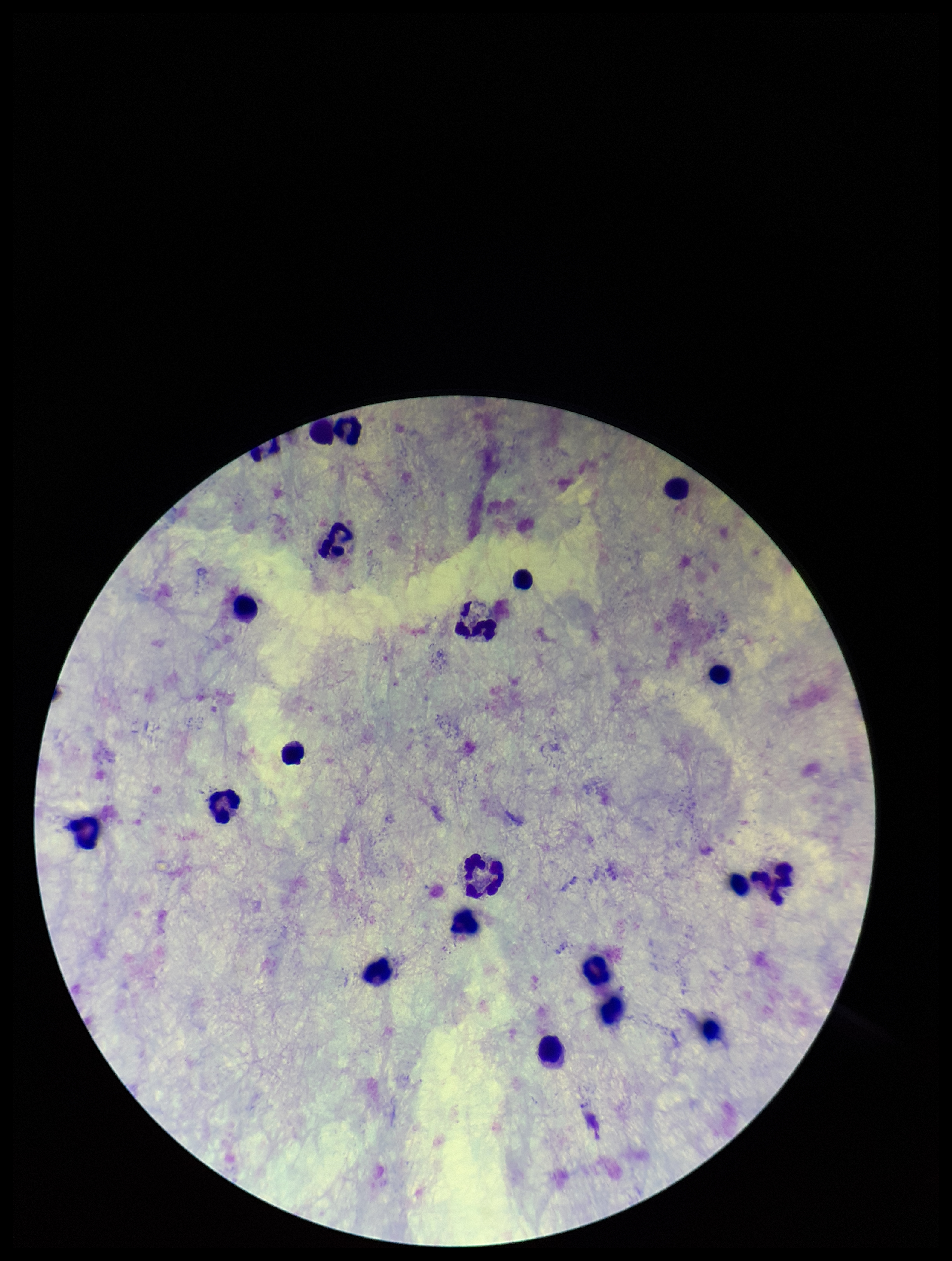
One field from this slide. Patient malaria status: negative. Parasite count: 0. Preparation: thick blood smear. Image is 952×1261 pixels. Plasmodium parasites: none detected. Leukocyte count: 21. Stained with Giemsa. Smartphone photograph taken through the eyepiece of a microscope.